Identify the parasite.
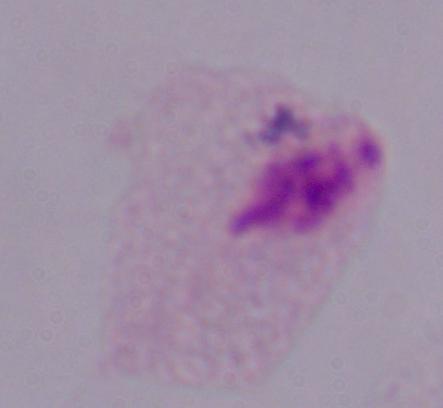
This is a trichomonad.

Summary:
  - Modality: photomicrograph
  - Magnification: 1000x